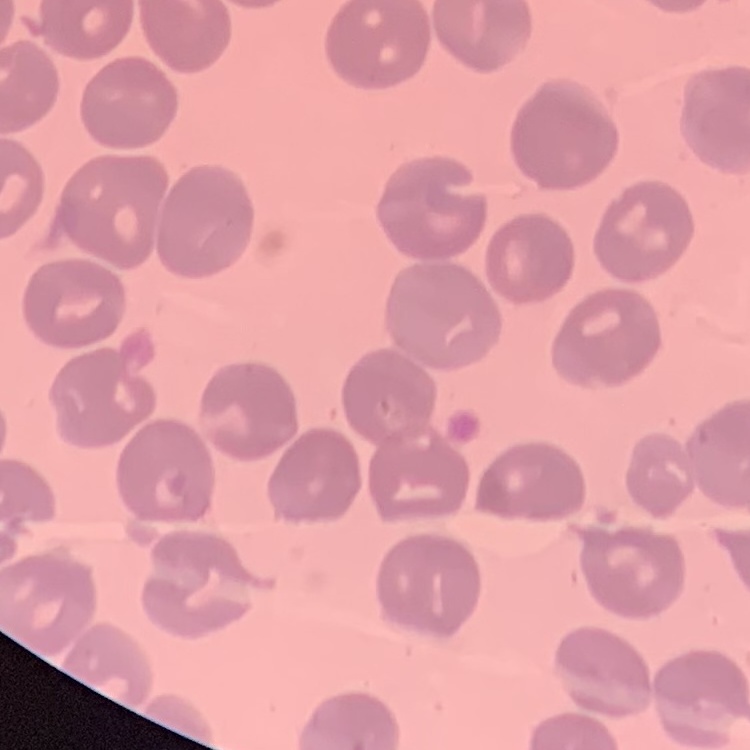

Summary:
  - Erythrocyte morphology: no rouleaux formation
  - Preparation: thin peripheral smear
  - Stain: Field's or Giemsa
  - Image type: square crop of a larger photomicrograph